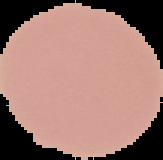

image size = 163×160 pixels
image type = segmented cell region on a black background
preparation = thin blood film
result = no Plasmodium parasites detected